Report the malaria status of this cell.
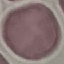

It is uninfected.

Summary:
  - Preparation: thin blood film
  - Image type: cell patch, automatically extracted from a larger field of view and resized to 64 × 64 pixels
  - Capture: smartphone through the microscope eyepiece
  - Stain: Giemsa